Give the position of every leukocyte visible.
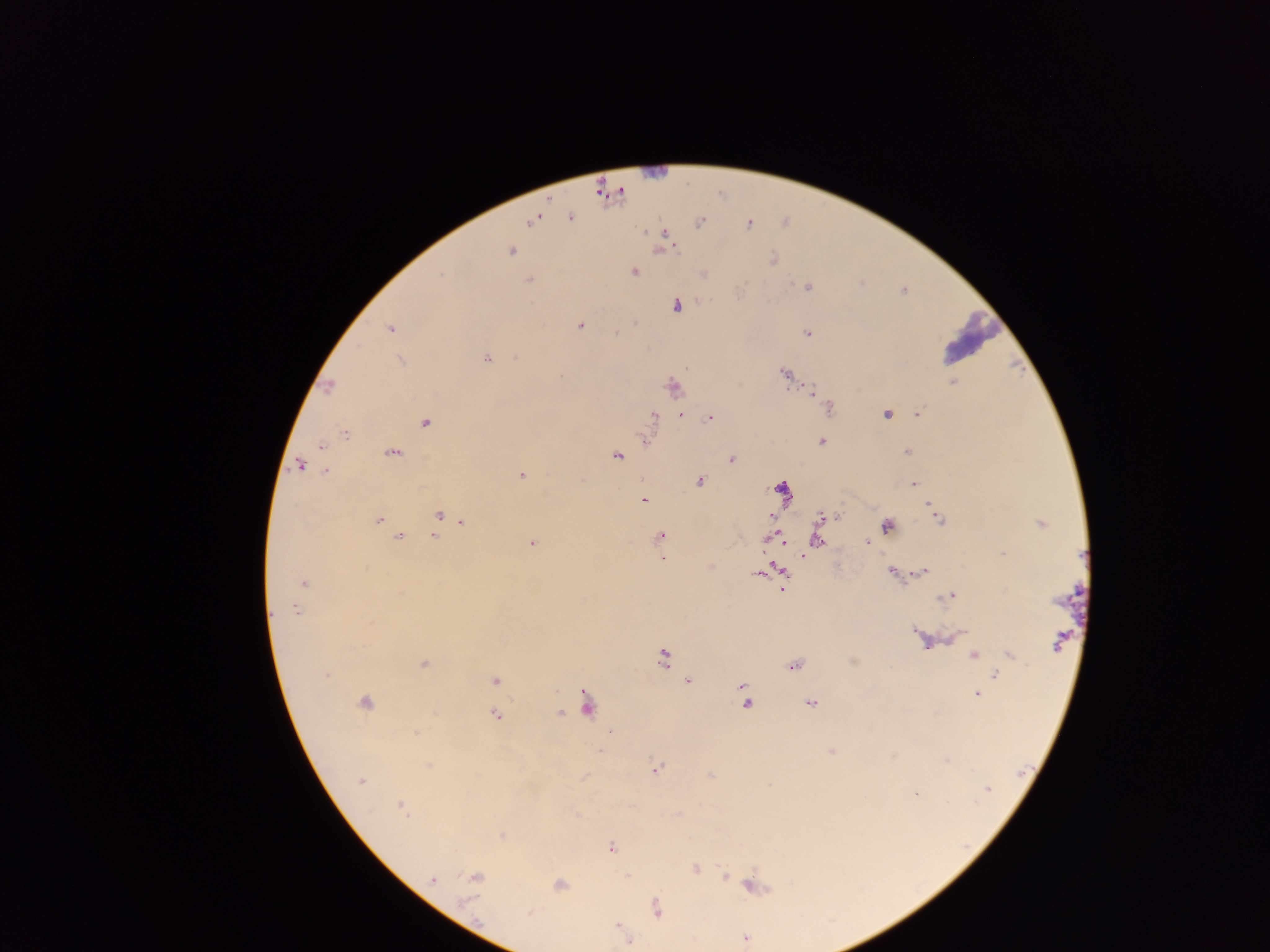

No leukocytes observed.

Plasmodium parasite locations = approximate centers as [x, y] in pixels (subset; some below the resolvable size): [749, 225], [644, 232], [663, 233], [657, 249], [510, 250], [634, 272], [440, 274], [529, 279], [742, 285], [806, 287], [676, 306], [580, 325], [390, 328], [615, 330], [806, 333], [362, 346], [486, 358], [783, 374], [561, 376], [785, 378], [953, 381], [329, 387], [671, 387], [812, 391], [654, 415], [682, 415], [885, 415], [917, 415], [708, 418], [424, 422], [344, 432], [821, 440], [320, 444], [907, 450], [392, 452], [616, 455], [732, 458], [299, 465], [326, 470], [521, 474], [700, 480], [913, 483], [643, 501], [927, 507], [438, 514], [838, 517], [818, 518], [378, 519], [772, 519], [462, 521], [1040, 523], [887, 527], [660, 535], [400, 536], [433, 536], [817, 539], [782, 542], [867, 543], [533, 544], [662, 559], [710, 566], [778, 569], [890, 571], [759, 575], [304, 584], [782, 591], [938, 599], [274, 610], [296, 610], [914, 632], [947, 640], [927, 645], [1056, 646], [1008, 654], [975, 656], [662, 658], [852, 661], [423, 663], [793, 666], [994, 674], [327, 676], [496, 679], [688, 680], [741, 685], [977, 693], [583, 702], [810, 703], [364, 704], [747, 704], [435, 711], [560, 712], [497, 714], [415, 732], [610, 733], [599, 749], [831, 752], [894, 755], [945, 760], [428, 767], [657, 767], [709, 773], [584, 777], [359, 782], [916, 794], [400, 804], [677, 814], [502, 836], [611, 848], [694, 868], [626, 875], [724, 875], [475, 876], [433, 880], [559, 884], [749, 885], [468, 898], [656, 907], [617, 925], [746, 939], [628, 941]
field of view = single
capture = mobile-phone photograph through a microscope
preparation = thick blood smear
country = Ghana
image size = 1270×952 pixels